Locate every Plasmodium falciparum-infected red blood cell.
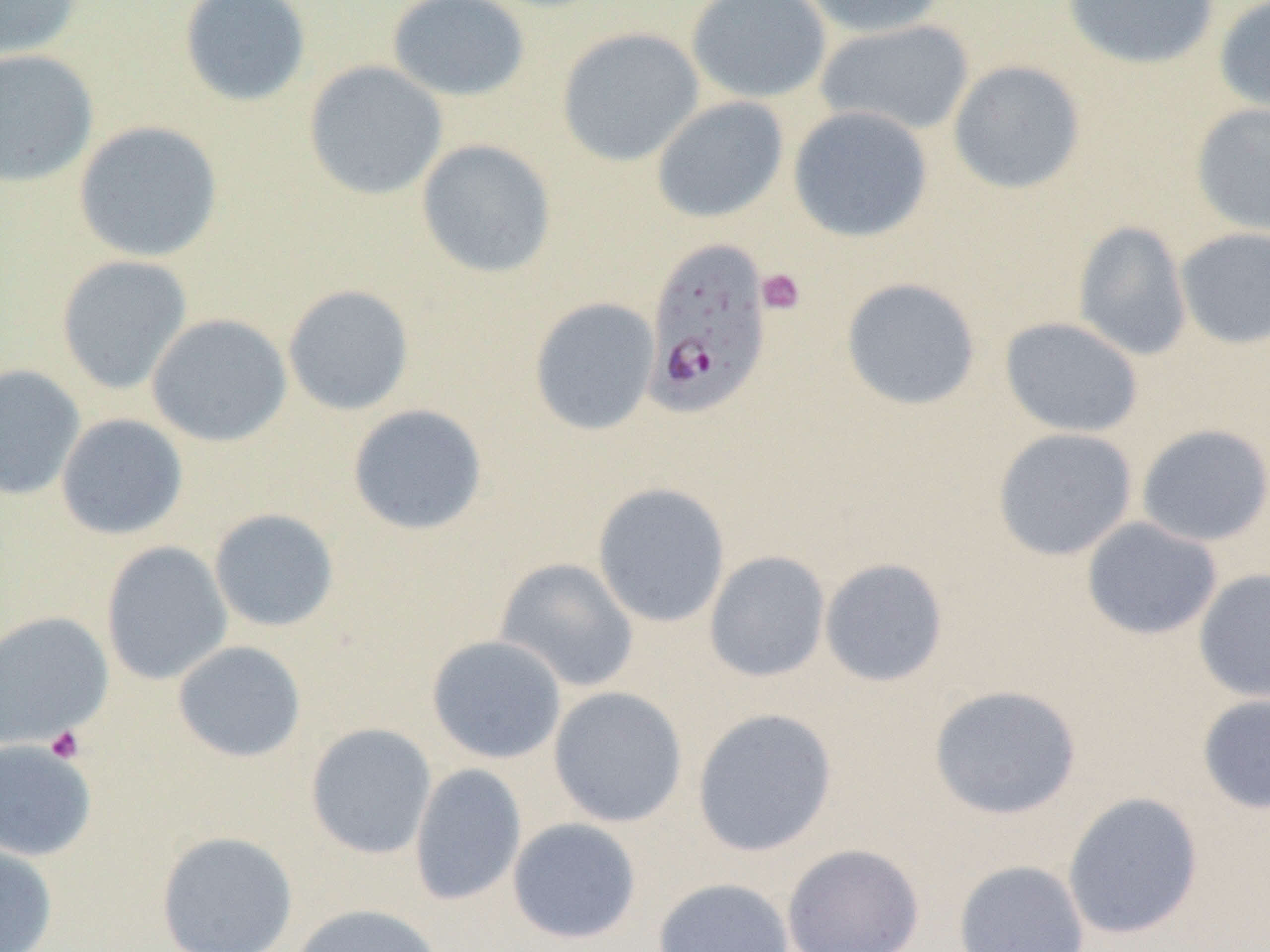

Approximate bounding boxes as (x1, y1, x2, y2) in pixels.
Plasmodium falciparum-infected red blood cells: (642, 237, 772, 419).

slide-level diagnosis = Plasmodium falciparum
magnification = 1000x
platelet locations = approximate bounding boxes as (x1, y1, x2, y2) in pixels: (756, 268, 806, 316), (46, 726, 85, 764)
uninfected red blood cell locations = approximate bounding boxes as (x1, y1, x2, y2) in pixels: (0, 0, 83, 61), (178, 0, 312, 108), (386, 0, 531, 102), (686, 0, 832, 104), (796, 0, 948, 38), (1061, 0, 1222, 71), (1212, 0, 1270, 119), (814, 18, 975, 137), (556, 26, 704, 167), (0, 49, 99, 188), (303, 60, 448, 200), (948, 60, 1086, 195), (651, 96, 789, 224), (1190, 102, 1270, 237), (787, 105, 933, 242), (72, 120, 224, 263), (415, 139, 556, 279), (1073, 220, 1192, 361), (1175, 227, 1270, 349), (56, 255, 193, 394), (840, 277, 981, 411), (282, 284, 415, 416), (529, 297, 660, 436), (146, 313, 292, 447), (1000, 317, 1143, 438), (0, 364, 86, 501), (347, 404, 488, 536), (55, 413, 188, 540), (1135, 423, 1270, 547), (992, 427, 1138, 561), (591, 482, 731, 629), (208, 508, 340, 633), (1080, 517, 1222, 641), (100, 541, 233, 686), (703, 550, 831, 683), (494, 556, 640, 693), (819, 557, 949, 688), (1193, 568, 1270, 704), (0, 610, 114, 748), (426, 635, 567, 764), (172, 640, 307, 763), (928, 684, 1082, 820), (548, 686, 688, 828), (1196, 692, 1270, 815), (691, 707, 838, 857), (305, 723, 437, 859), (0, 738, 98, 862), (409, 763, 527, 906), (1062, 791, 1204, 940), (507, 817, 642, 944), (155, 830, 298, 952), (0, 843, 58, 952), (781, 843, 925, 952), (953, 859, 1090, 952), (652, 877, 795, 952), (290, 903, 445, 952)
field of view = single
preparation = thin blood film
modality = light microscopy
image size = 1270×952 pixels